Identify the cell.
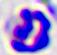
A leukocyte.

Captured at 400x magnification. Micrograph.